Comment on the morphology of the erythrocytes.
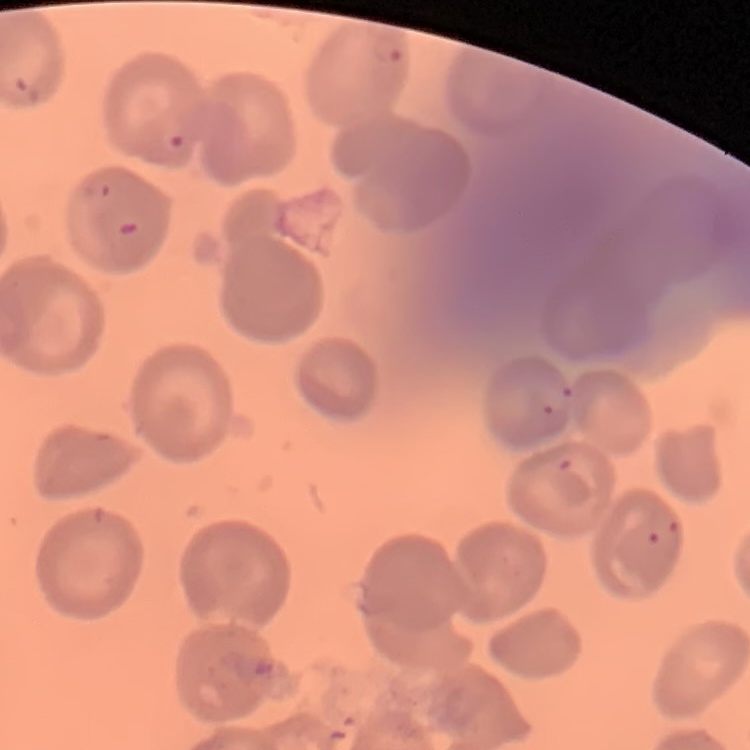

They show no rouleaux formation.

Summary:
  - Stain: Field's or Giemsa
  - Preparation: thin blood smear
  - Image type: one tile cut from a larger photomicrograph